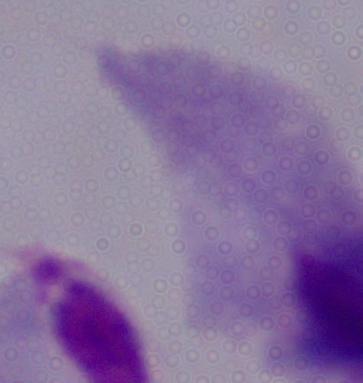
A trichomonad is shown. Micrograph. Captured at 1000x magnification.